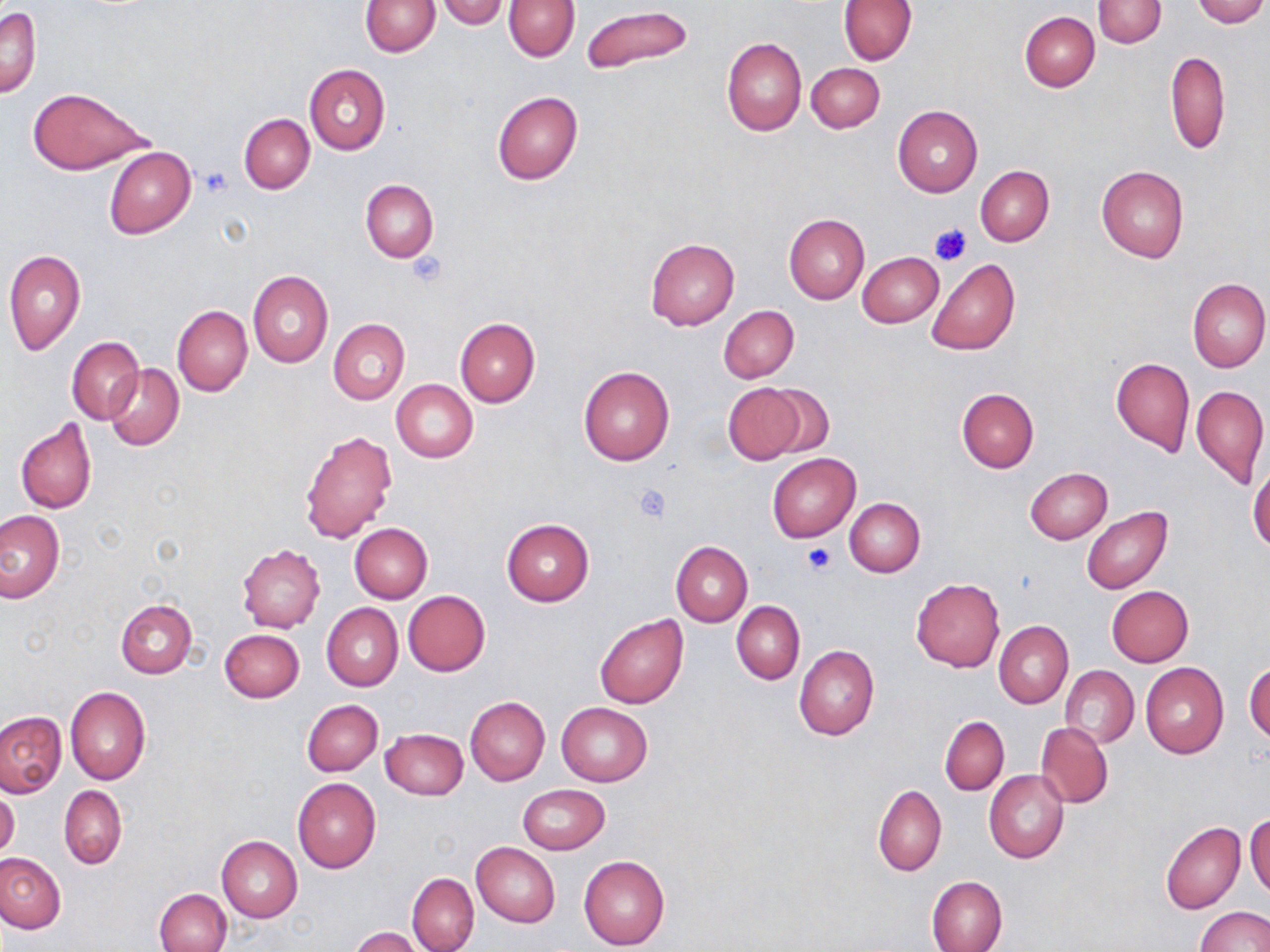
Approximate bounding boxes as (x1, y1, x2, y2) in pixels. Platelet locations: (203, 168, 232, 195), (929, 224, 971, 266), (404, 253, 448, 289), (632, 483, 672, 524), (803, 544, 837, 574). Uninfected red blood cell locations: (360, 0, 441, 56), (436, 0, 510, 28), (837, 0, 917, 65), (1093, 0, 1166, 47), (1192, 0, 1267, 26), (504, 1, 580, 61), (580, 4, 694, 75), (1, 6, 41, 97), (1019, 12, 1099, 91), (722, 37, 806, 135), (1165, 51, 1230, 154), (806, 62, 885, 133), (304, 63, 390, 154), (27, 88, 152, 174), (492, 90, 582, 185), (892, 106, 983, 197), (239, 114, 315, 193), (105, 146, 196, 239), (976, 165, 1053, 246), (1097, 166, 1188, 262), (361, 180, 439, 262), (783, 212, 869, 304), (646, 237, 740, 330), (2, 249, 86, 356), (857, 251, 944, 327), (926, 257, 1020, 356), (248, 271, 333, 369), (1187, 277, 1269, 373), (172, 305, 252, 397), (718, 305, 799, 384), (454, 317, 540, 407), (328, 319, 410, 404), (67, 336, 144, 425), (1111, 357, 1194, 457), (103, 364, 184, 450), (579, 366, 675, 467), (390, 379, 478, 463), (723, 384, 804, 463), (760, 384, 835, 460), (1191, 384, 1268, 490), (956, 387, 1039, 472), (16, 418, 98, 514), (298, 428, 397, 544), (767, 453, 860, 542), (1248, 459, 1269, 557), (1025, 467, 1113, 544), (845, 497, 925, 576), (1081, 506, 1173, 594), (0, 510, 64, 602), (501, 518, 594, 607), (349, 523, 433, 603), (670, 541, 753, 626), (237, 544, 325, 633), (911, 578, 1004, 672), (1106, 586, 1193, 666), (403, 590, 491, 675), (115, 599, 196, 678), (732, 600, 804, 684), (321, 603, 403, 691), (594, 615, 688, 709), (995, 621, 1073, 708), (220, 628, 304, 702), (794, 645, 879, 740), (1246, 662, 1270, 744), (1141, 663, 1229, 759), (1061, 665, 1139, 748), (65, 686, 150, 785), (464, 696, 550, 787), (302, 699, 383, 776), (557, 702, 652, 786), (0, 712, 68, 797), (940, 716, 1009, 795), (1036, 723, 1113, 808), (380, 727, 468, 799), (985, 770, 1069, 863), (292, 777, 381, 873), (517, 783, 611, 855), (873, 783, 947, 876), (58, 785, 127, 870), (0, 790, 20, 859), (1246, 810, 1269, 896), (1161, 821, 1245, 915), (216, 836, 302, 922), (471, 843, 560, 926), (0, 852, 67, 933), (578, 854, 670, 950), (406, 873, 479, 952), (927, 876, 1007, 952), (155, 888, 231, 951), (1196, 906, 1269, 952), (349, 927, 421, 952). Slide-level diagnosis: negative for blood parasites. One field of a larger specimen. May-Grünwald-Giemsa-stained preparation. Image is 1270×952 pixels. Light microscopy. Thin blood film. 1000x magnification.